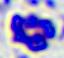

Captured at 400x magnification. A white blood cell is seen. Photomicrograph.